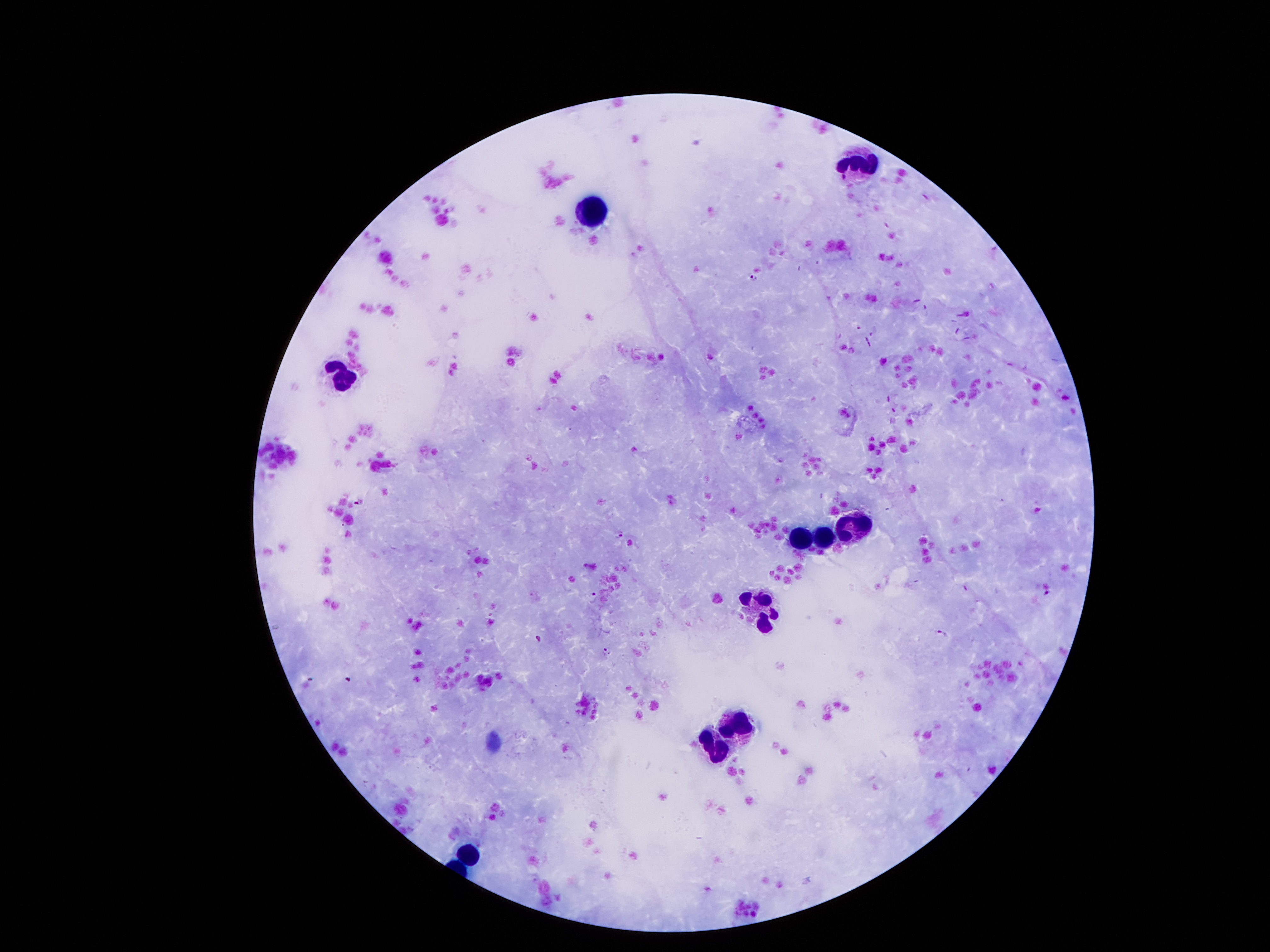
Approximate centers as (x, y) in pixels. Leukocyte locations: (861, 170), (593, 210), (341, 379), (853, 525), (821, 540), (800, 543), (767, 605), (740, 723), (719, 746), (467, 857). Malaria parasite locations: (754, 279), (357, 503), (618, 534), (1047, 593), (593, 596), (941, 633), (538, 638), (607, 652). Photographed through the microscope eyepiece with a smartphone camera. Giemsa-stained preparation. Thick blood smear. One field from this slide. Image is 1270×952 pixels. 100x magnification. Patient malaria status: infected with Plasmodium falciparum.